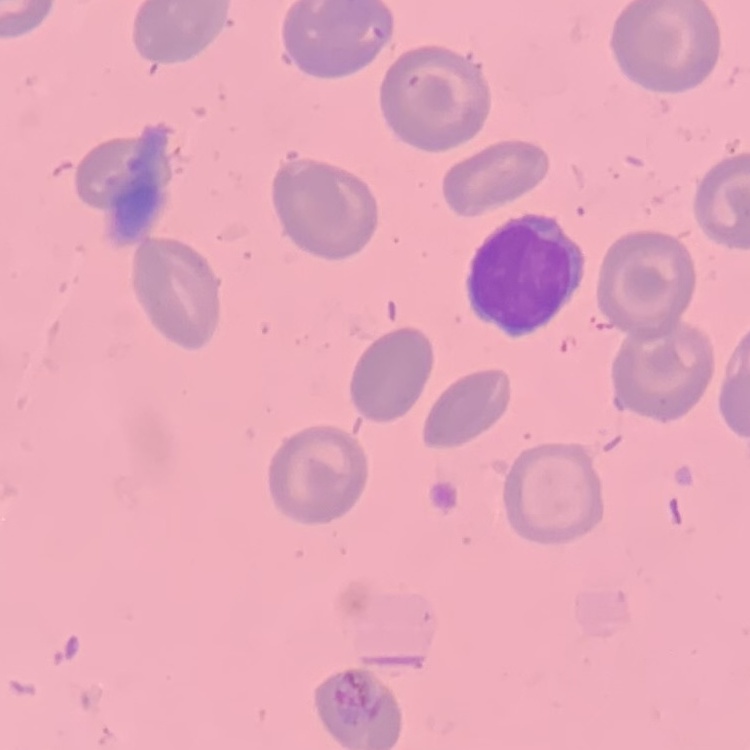

The red blood cells show no rouleaux formation. Thin blood film. Stained with either Field's or Giemsa. One tile cut from a larger photomicrograph.